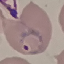
Malaria status: parasitized. Acquired by smartphone through the microscope eyepiece. Giemsa stain. Thin blood film. Cell patch, automatically extracted from a larger field of view and resized to 64 × 64 pixels.